Identify the blood parasite species.
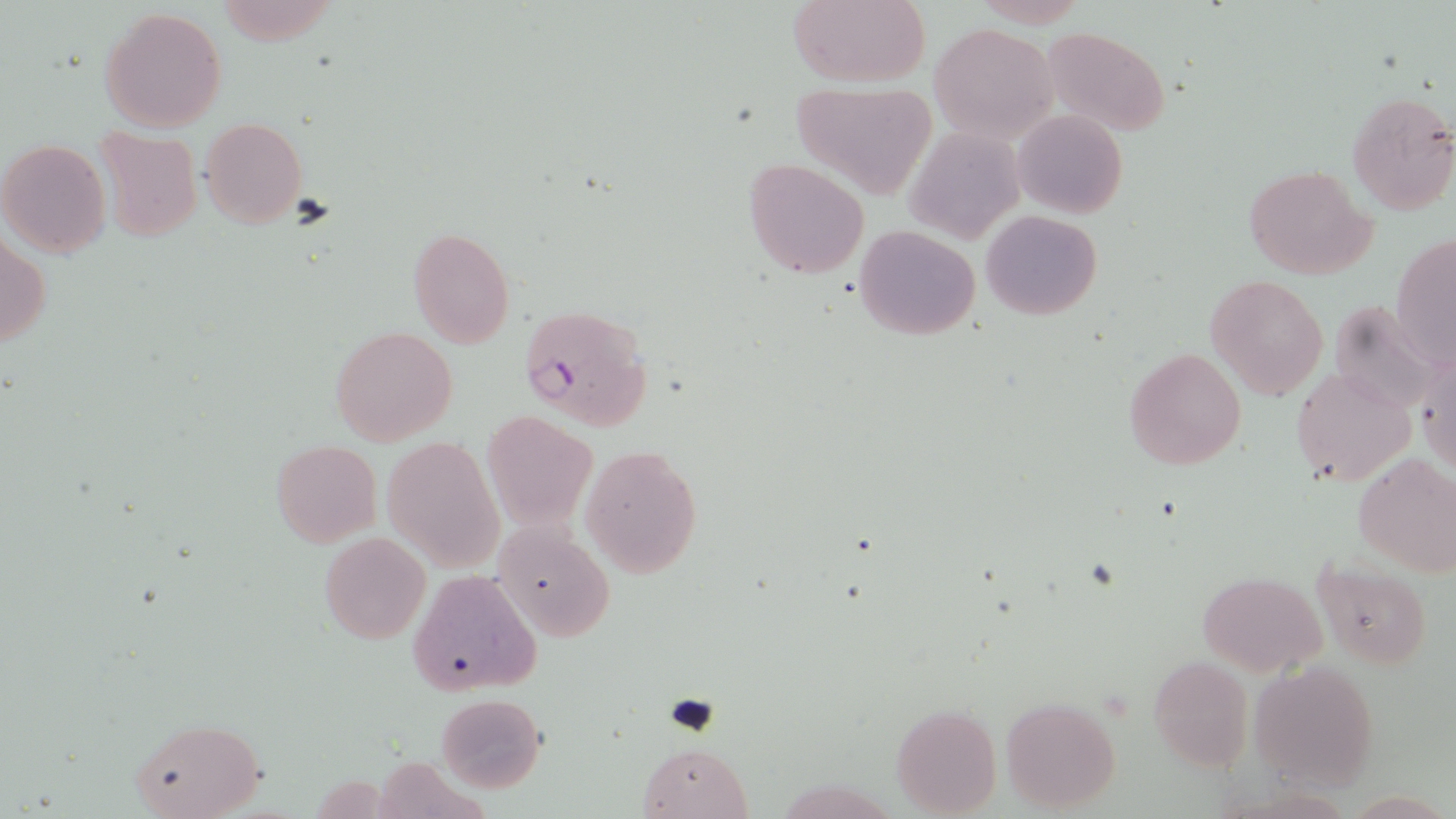
Plasmodium falciparum.

Summary:
  - Coordinate format: approximate bounding boxes as (x1, y1, x2, y2) in pixels
  - Plasmodium falciparum-infected red blood cell locations: (519, 304, 651, 429)
  - Uninfected red blood cell locations: (215, 0, 343, 46), (786, 0, 933, 87), (99, 7, 227, 133), (928, 22, 1060, 143), (1041, 29, 1173, 136), (790, 81, 936, 201), (1344, 89, 1456, 216), (1012, 108, 1127, 219), (200, 117, 307, 228), (905, 124, 1024, 245), (94, 127, 201, 243), (1, 139, 112, 257), (743, 156, 870, 278), (1244, 164, 1376, 280), (981, 210, 1102, 320), (853, 226, 981, 339), (406, 227, 515, 348), (1, 233, 49, 347), (1390, 233, 1455, 368), (1206, 273, 1329, 400), (1328, 299, 1445, 414), (330, 327, 457, 447), (1414, 340, 1456, 479), (1123, 347, 1246, 469), (1290, 366, 1416, 485), (481, 411, 597, 529), (383, 436, 505, 572), (271, 440, 381, 548), (580, 444, 704, 578), (1353, 453, 1456, 576), (494, 521, 615, 641), (319, 532, 431, 644), (1310, 559, 1434, 670), (408, 570, 542, 695), (1198, 571, 1327, 676), (1147, 655, 1254, 774), (1250, 660, 1381, 789), (434, 693, 546, 794), (1001, 696, 1121, 813), (890, 704, 1001, 817), (129, 717, 265, 819), (636, 741, 754, 819)
  - Field of view: single
  - Stain: May-Grünwald-Giemsa
  - Image size: 1456×819 pixels
  - Preparation: thin blood film
  - Modality: light microscopy
  - Magnification: 1000x